Assess this cell for malaria.
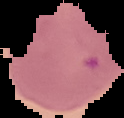

It is parasitized.

image type = segmented cell region on a black background
preparation = thin blood film
image size = 124×118 pixels